Name the blood parasite species.
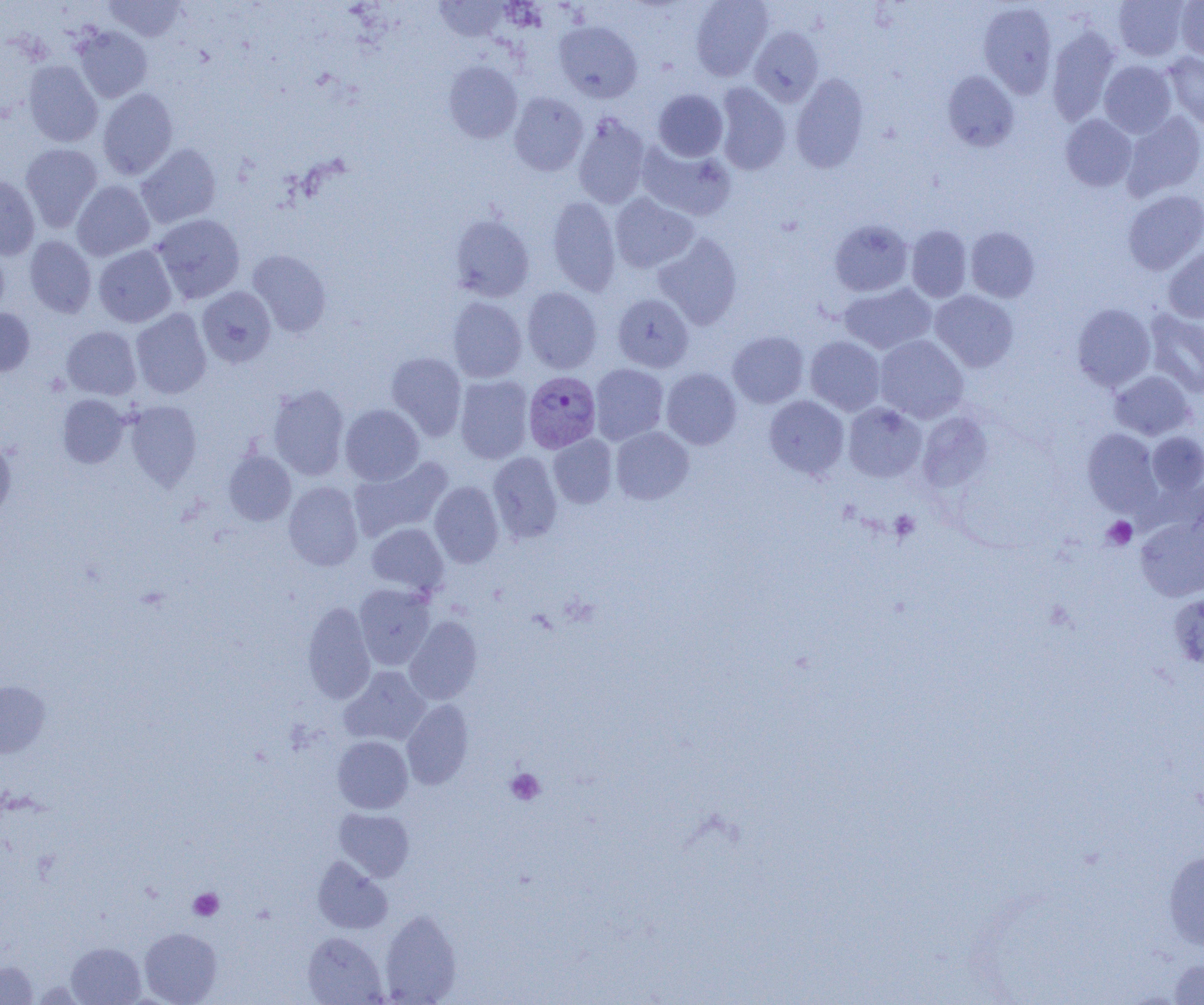

Plasmodium vivax.

{
  "platelet_locations": "approximate bounding boxes as (x1, y1, x2, y2) in pixels: (889, 510, 920, 543), (1103, 516, 1137, 549), (505, 768, 545, 805), (189, 888, 223, 920)",
  "image_size": "1204×1005 pixels",
  "magnification": "1000x",
  "modality": "light microscopy",
  "plasmodium_vivax_infected_red_blood_cell_locations": "approximate bounding boxes as (x1, y1, x2, y2) in pixels: (523, 371, 600, 453)",
  "preparation": "thin blood film",
  "field_of_view": "one of a larger specimen",
  "uninfected_red_blood_cell_locations": "approximate bounding boxes as (x1, y1, x2, y2) in pixels: (104, 0, 187, 41), (434, 0, 511, 42), (690, 0, 773, 80), (1113, 0, 1189, 61), (1175, 0, 1204, 61), (978, 2, 1057, 98), (554, 21, 642, 102), (74, 26, 153, 102), (1046, 26, 1120, 125), (749, 27, 823, 106), (1164, 52, 1204, 131), (1099, 60, 1176, 137), (23, 61, 102, 147), (443, 61, 523, 143), (942, 71, 1019, 151), (790, 73, 869, 173), (713, 83, 791, 174), (97, 88, 178, 180), (653, 89, 728, 161), (509, 92, 588, 176), (1123, 111, 1204, 199), (572, 113, 651, 208), (1061, 114, 1137, 191), (638, 142, 736, 221), (20, 143, 103, 232), (136, 144, 222, 228), (0, 174, 40, 260), (72, 180, 155, 261), (1123, 189, 1204, 275), (610, 193, 699, 273), (548, 196, 621, 296), (152, 214, 245, 303), (450, 214, 534, 301), (829, 220, 913, 296), (906, 226, 972, 302), (965, 227, 1039, 302), (653, 233, 742, 329), (24, 235, 96, 318), (0, 244, 9, 322), (93, 245, 177, 327), (1163, 246, 1204, 323), (247, 250, 331, 337), (839, 283, 936, 354), (197, 286, 276, 367), (522, 287, 602, 373), (930, 290, 1018, 372), (612, 293, 694, 372), (447, 297, 527, 382), (1072, 304, 1156, 392), (0, 308, 34, 376), (130, 308, 212, 399), (1145, 309, 1204, 398), (61, 326, 141, 400), (728, 331, 809, 408), (874, 335, 969, 423), (805, 337, 885, 415), (386, 351, 467, 440), (589, 363, 668, 445), (661, 368, 741, 449), (1109, 371, 1195, 440), (454, 375, 533, 463), (268, 384, 350, 480), (57, 394, 130, 468), (764, 395, 849, 478), (125, 400, 202, 490), (843, 402, 927, 482), (340, 404, 424, 485), (917, 411, 993, 492), (611, 426, 694, 504), (1083, 428, 1162, 516), (1146, 432, 1204, 496), (548, 434, 617, 508), (0, 437, 16, 521), (223, 449, 296, 525), (488, 451, 563, 543), (349, 455, 453, 541), (283, 481, 363, 570), (430, 481, 503, 567), (1136, 514, 1204, 602), (366, 523, 449, 596), (353, 584, 436, 669), (1169, 593, 1204, 669), (302, 602, 376, 703), (404, 616, 483, 704), (340, 666, 430, 746), (0, 681, 51, 757), (401, 699, 473, 789), (333, 735, 413, 813), (334, 808, 415, 881), (1163, 849, 1204, 952), (312, 857, 392, 934), (379, 909, 461, 1005), (140, 927, 222, 1004), (302, 932, 386, 1004), (66, 942, 145, 1005), (1167, 957, 1204, 1004), (0, 961, 37, 1004)"
}